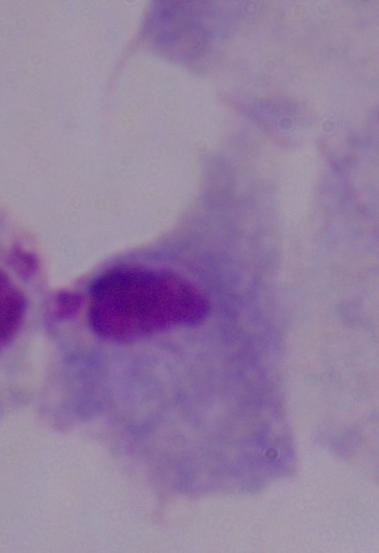

modality = micrograph
magnification = 1000x
identification = trichomonad